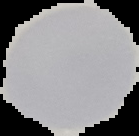

Summary:
  - Image size: 139×136 pixels
  - Image type: cell region segmented out of the field of view; surrounding area masked to black
  - Preparation: thin blood smear
  - Malaria status: uninfected